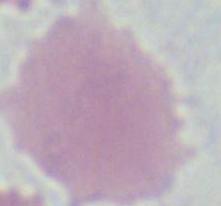
magnification = 1000x
modality = micrograph
identification = red blood cell